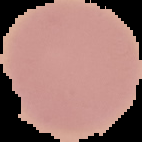

image_type: segmented cell region on a black background
malaria_status: uninfected
preparation: thin blood smear
image_size: 142×142 pixels